State which parasite is depicted.
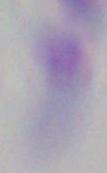

This is Toxoplasma gondii.

1000x magnification. Micrograph.